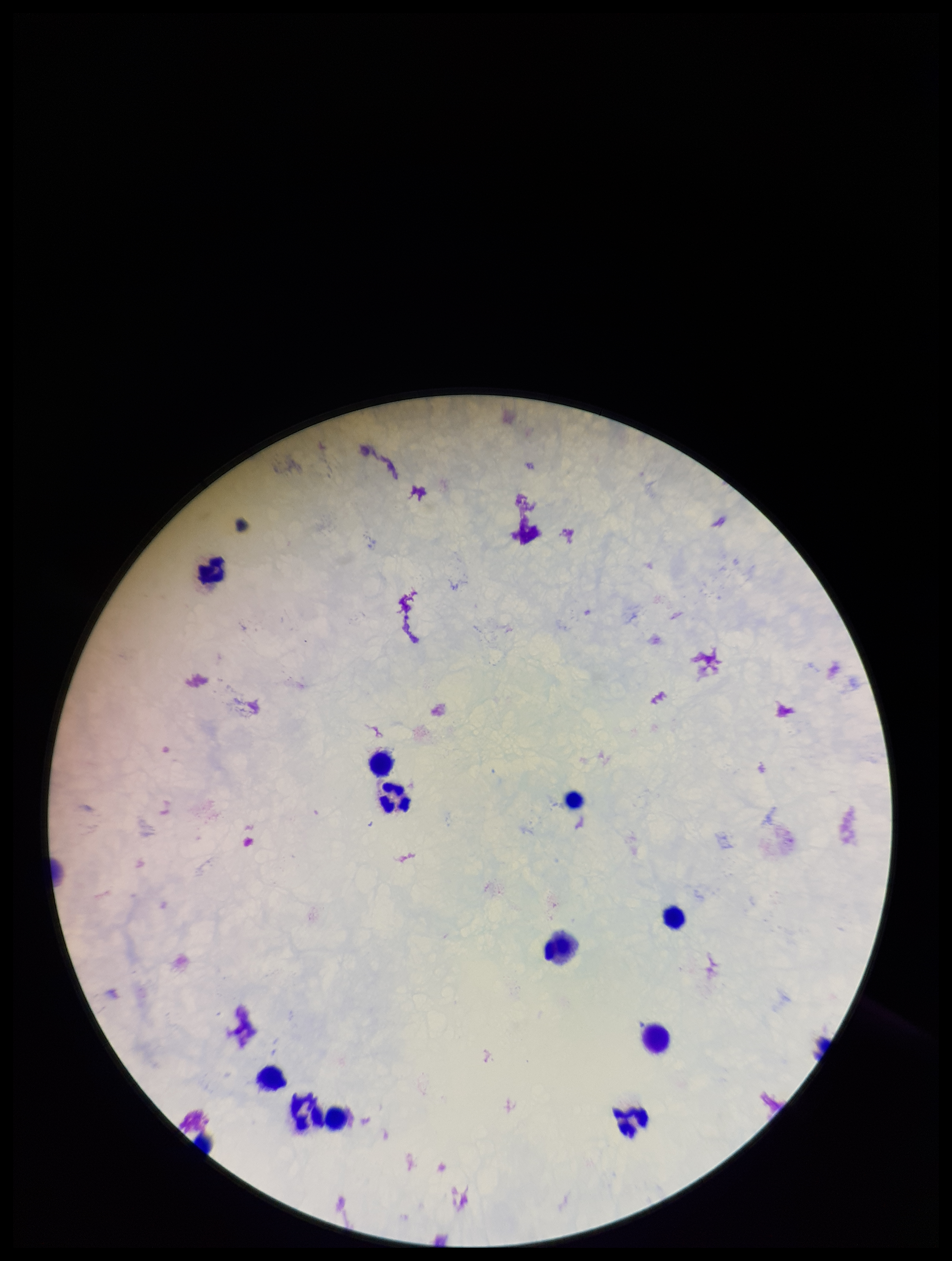

Image is 952×1261 pixels. Plasmodium parasites: none detected. Giemsa stain. Single field of view. Photographed through the microscope eyepiece with a smartphone camera. Parasite count: 0. Preparation: thick. Patient malaria status: negative. Leukocyte count: 12.